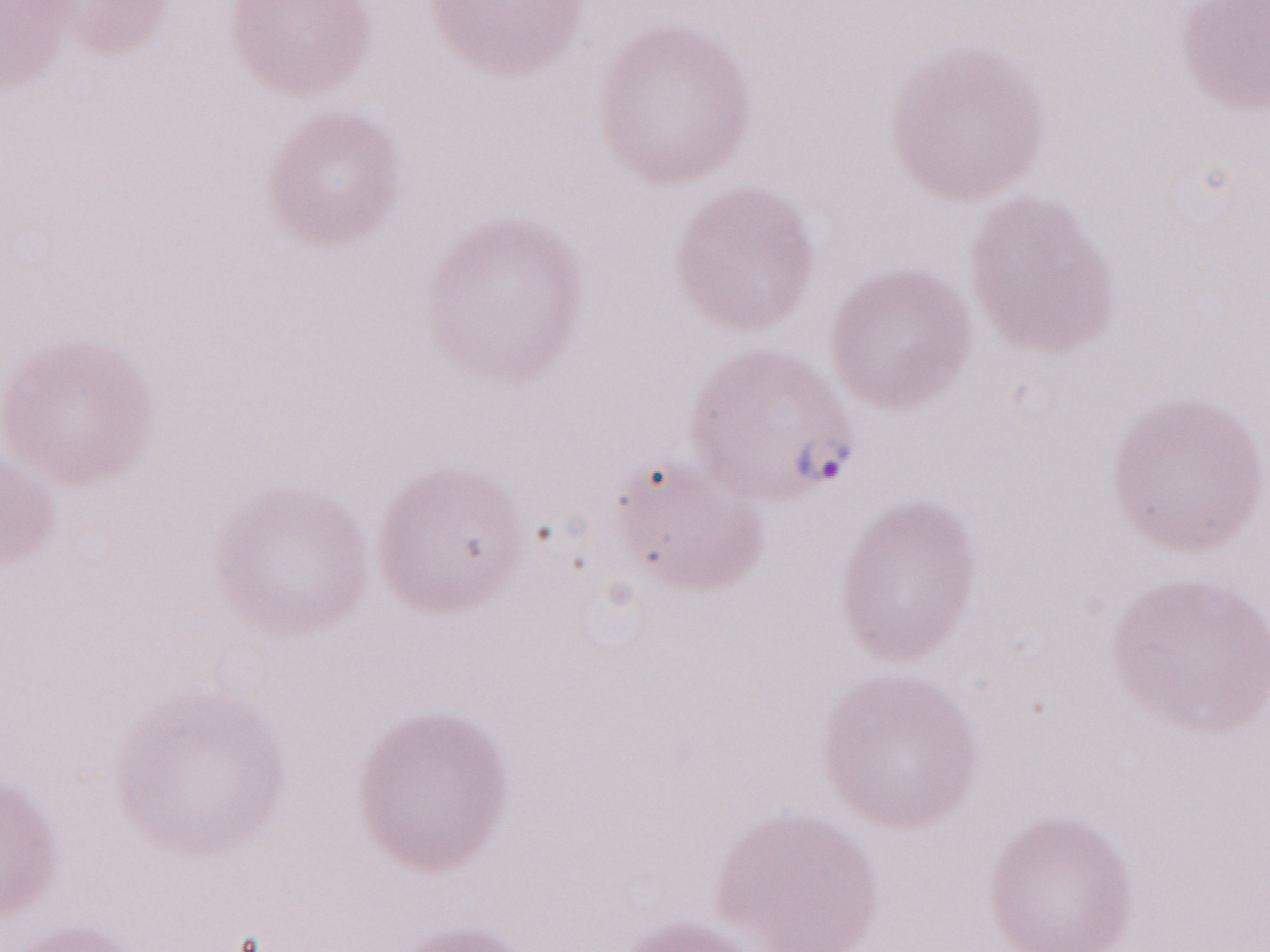
Olympus BX43 microscope and DP73 digital camera. Image is 1270×952 pixels. May-Grünwald-Giemsa-stained preparation. 1,000x magnification. Patient diagnosis: malaria infection. One field of this slide. Thin peripheral-blood smear.